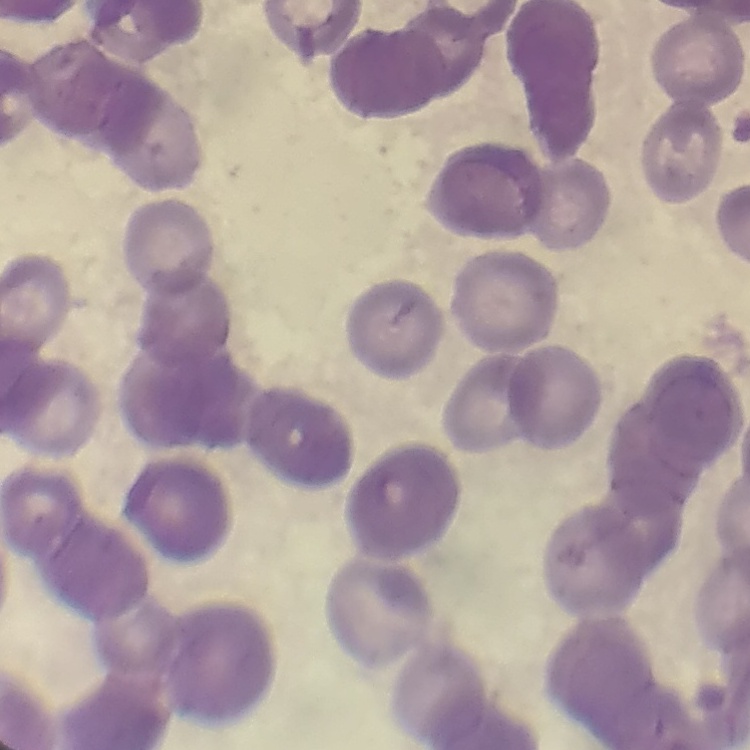

Summary:
  - Erythrocyte morphology: rouleaux formation
  - Preparation: thin blood film
  - Image type: square crop of a larger photomicrograph
  - Stain: Field's or Giemsa